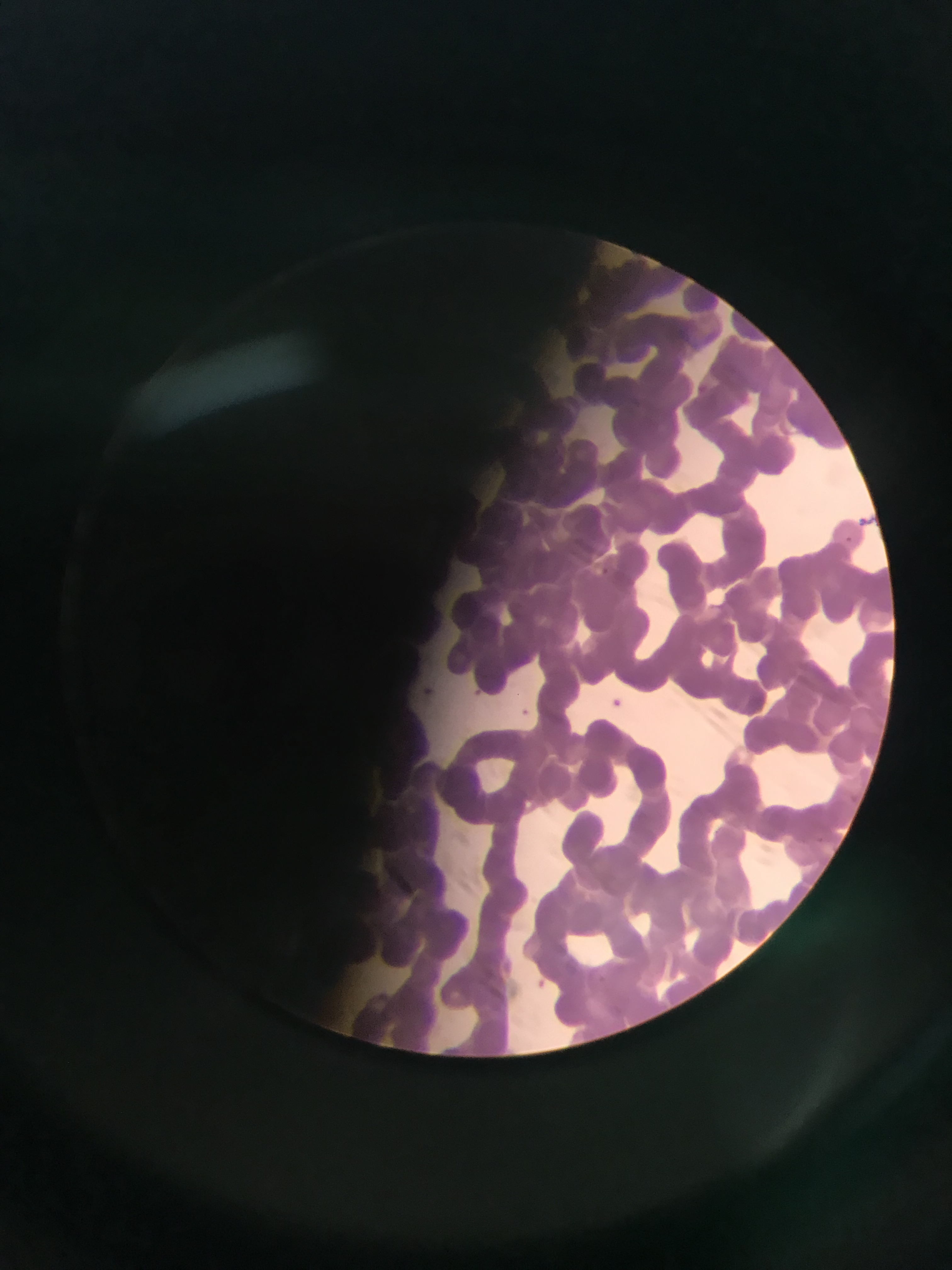
{
  "preparation": "thin blood smear",
  "image_size": "952×1270 pixels",
  "capture": "mobile-phone photograph through a microscope",
  "country": "Ghana",
  "field_of_view": "single",
  "plasmodium_parasite_locations": "approximate bounding boxes as [left, top, right, bottom] in pixels: [857, 513, 876, 533], [845, 532, 861, 554], [595, 564, 610, 583], [606, 688, 631, 711]"
}